State the blood parasite species.
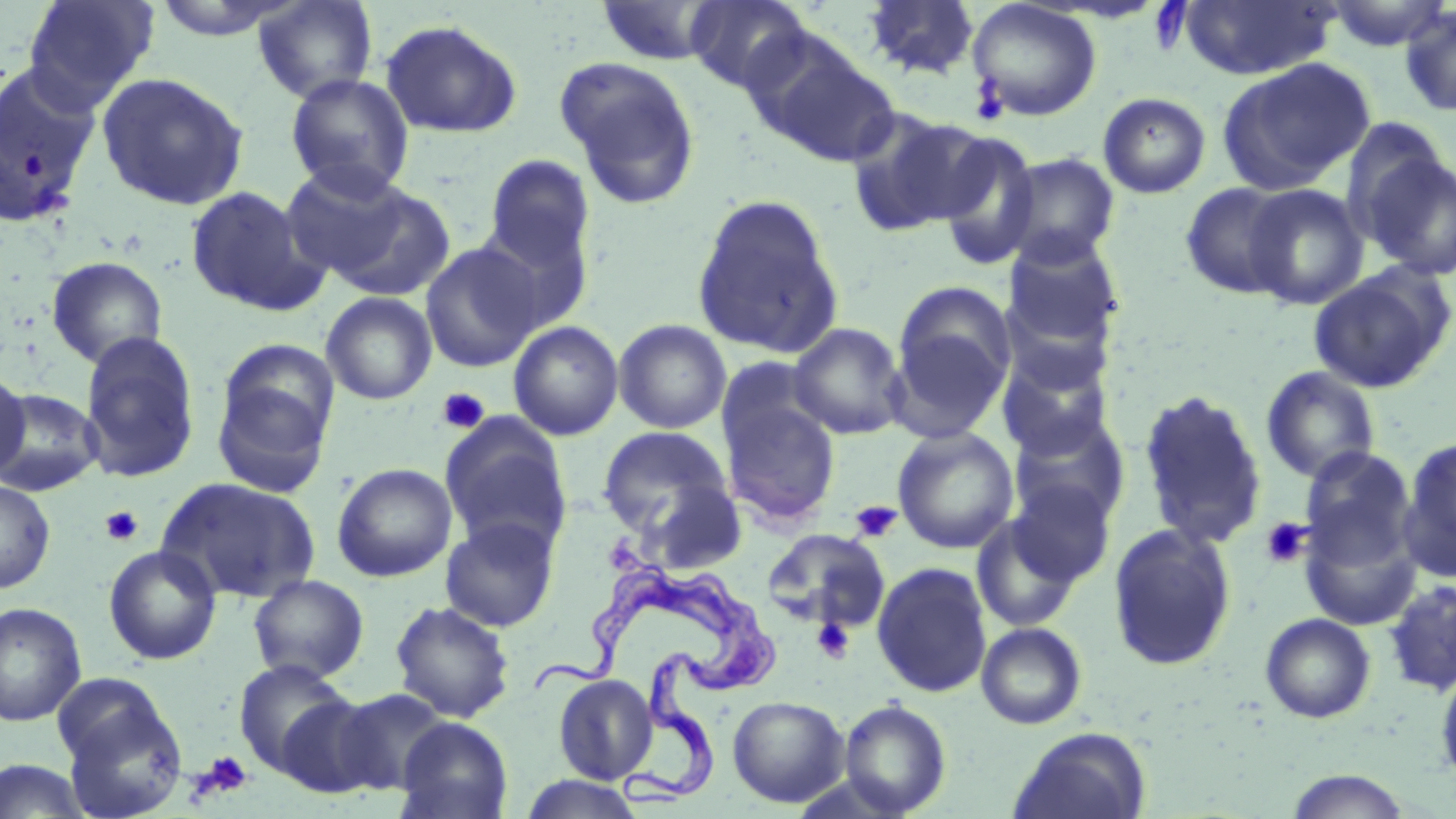
Trypanosoma brucei.

Summary:
  - Coordinate format: approximate bounding boxes as [x1, y1, x2, y2] in pixels
  - Uninfected red blood cell locations: [22, 0, 159, 107], [149, 0, 303, 41], [252, 0, 379, 104], [685, 0, 812, 94], [861, 0, 982, 81], [967, 0, 1103, 122], [1323, 0, 1452, 51], [596, 1, 725, 65], [1179, 1, 1337, 80], [1398, 5, 1456, 117], [380, 19, 523, 138], [745, 29, 899, 168], [555, 57, 702, 208], [1217, 57, 1375, 194], [0, 62, 103, 225], [96, 71, 250, 210], [284, 74, 415, 198], [1098, 92, 1211, 199], [842, 107, 987, 237], [932, 130, 1044, 272], [1353, 139, 1456, 282], [1000, 152, 1121, 268], [483, 155, 595, 272], [279, 162, 415, 280], [1180, 181, 1300, 300], [326, 183, 457, 301], [1242, 184, 1369, 309], [184, 185, 327, 317], [692, 194, 844, 358], [475, 211, 595, 334], [1002, 234, 1124, 352], [420, 242, 545, 373], [46, 256, 168, 369], [1308, 266, 1454, 394], [893, 281, 1016, 407], [321, 292, 437, 405], [613, 319, 732, 434], [508, 320, 624, 441], [788, 322, 909, 440], [78, 331, 201, 483], [996, 349, 1113, 460], [715, 356, 823, 460], [1260, 366, 1381, 484], [0, 368, 30, 481], [211, 373, 334, 498], [0, 388, 103, 496], [1137, 389, 1268, 550], [720, 397, 841, 527], [1007, 413, 1129, 527], [438, 414, 572, 555], [597, 425, 733, 537], [892, 426, 1019, 554], [1397, 436, 1456, 582], [1299, 447, 1418, 571], [331, 462, 458, 582], [158, 476, 322, 604], [640, 477, 747, 574], [0, 479, 55, 594], [1005, 479, 1116, 588], [971, 512, 1086, 633], [1298, 513, 1423, 632], [440, 516, 560, 632], [1107, 522, 1237, 671], [762, 528, 889, 631], [103, 544, 221, 665], [871, 561, 993, 698], [247, 574, 369, 684], [1384, 579, 1456, 696], [389, 600, 515, 723], [0, 602, 87, 727], [1259, 613, 1376, 723], [976, 622, 1087, 730], [233, 658, 354, 776], [1434, 666, 1456, 788], [553, 674, 658, 784], [54, 678, 188, 817], [332, 687, 451, 795], [726, 695, 850, 807], [275, 697, 383, 798], [838, 699, 952, 817], [395, 717, 513, 819], [1009, 726, 1152, 819], [0, 760, 94, 818], [1284, 769, 1415, 818], [518, 774, 648, 818]
  - Platelet locations: [969, 77, 1010, 127], [437, 387, 491, 434], [850, 500, 902, 542], [100, 505, 144, 547], [1259, 517, 1312, 569], [812, 618, 855, 663], [195, 750, 254, 800]
  - Trypanosoma brucei locations: [537, 559, 786, 807]
  - Magnification: 1000x
  - Modality: optical microscopy
  - Image size: 1456×819 pixels
  - Field of view: single
  - Stain: May-Grünwald-Giemsa
  - Preparation: thin blood smear